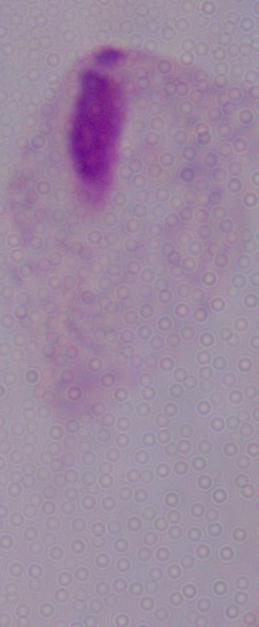
Photomicrograph. Captured at 1000x magnification. A trichomonad is seen.